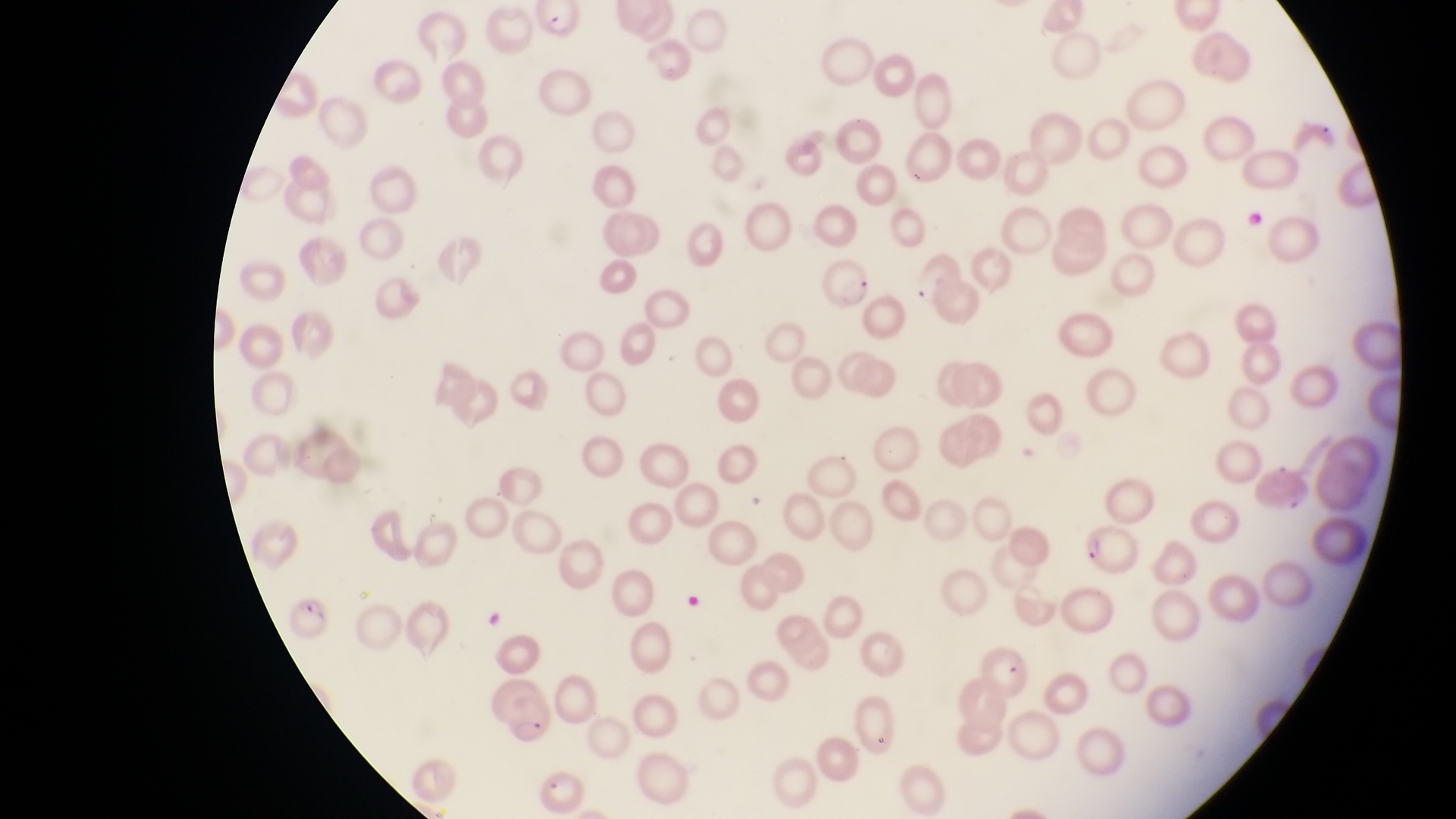
{
  "magnification": "1000x",
  "country": "Uganda",
  "parasitised_red_blood_cell_locations": "approximate bounding boxes as left top right bottom in pixels: 531 2 595 42; 816 254 874 309; 1078 523 1150 576; 281 589 341 648; 489 680 558 751; 536 764 589 816",
  "field_of_view": "single",
  "preparation": "thin blood smear",
  "image_size": "1456×819 pixels",
  "capture": "smartphone photograph through the eyepiece of an Olympus CX-23 microscope"
}